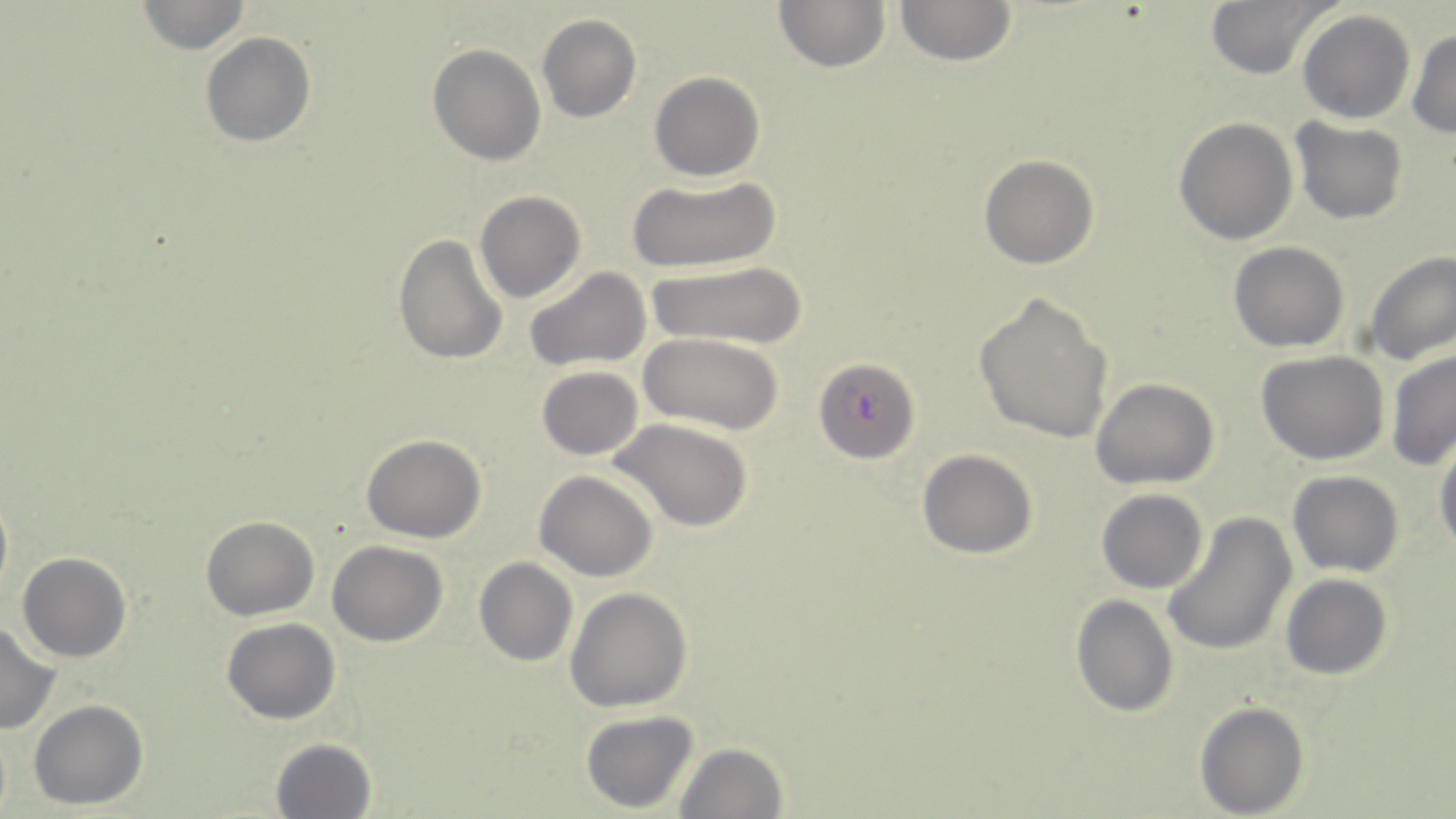

Approximate bounding boxes as [x1, y1, x2, y2] in pixels. Uninfected red blood cell locations: [134, 0, 253, 54], [773, 0, 891, 73], [893, 0, 1019, 67], [1202, 0, 1340, 81], [1298, 11, 1415, 123], [536, 16, 641, 122], [1407, 28, 1455, 139], [200, 31, 316, 148], [427, 44, 545, 166], [649, 71, 764, 181], [1173, 117, 1297, 245], [1292, 118, 1409, 222], [979, 155, 1100, 270], [624, 174, 782, 274], [473, 191, 585, 303], [392, 232, 508, 365], [1228, 242, 1349, 351], [1363, 250, 1455, 366], [645, 263, 807, 349], [524, 266, 652, 373], [971, 288, 1115, 443], [641, 334, 783, 435], [1383, 348, 1456, 470], [1256, 349, 1389, 464], [536, 365, 642, 461], [1092, 378, 1219, 489], [612, 418, 753, 532], [361, 433, 486, 543], [1433, 436, 1456, 552], [918, 450, 1037, 558], [534, 470, 658, 581], [1287, 470, 1406, 577], [0, 482, 12, 607], [1096, 489, 1206, 594], [1160, 513, 1296, 658], [200, 515, 320, 621], [326, 540, 449, 646], [16, 552, 132, 663], [475, 558, 577, 667], [1279, 574, 1393, 682], [565, 587, 692, 712], [1069, 593, 1178, 719], [223, 618, 340, 724], [0, 622, 61, 734], [29, 700, 149, 811], [1193, 701, 1310, 817], [580, 711, 701, 813], [0, 723, 12, 819], [269, 737, 377, 819], [673, 742, 787, 819]. Plasmodium falciparum-infected red blood cell locations: [813, 355, 920, 463]. Slide-level diagnosis: Plasmodium falciparum. Optical microscopy. Image is 1456×819 pixels. May-Grünwald-Giemsa stain. Thin blood film. Captured at 1000x magnification. Single field of view.